Point out each malaria parasite and each leukocyte.
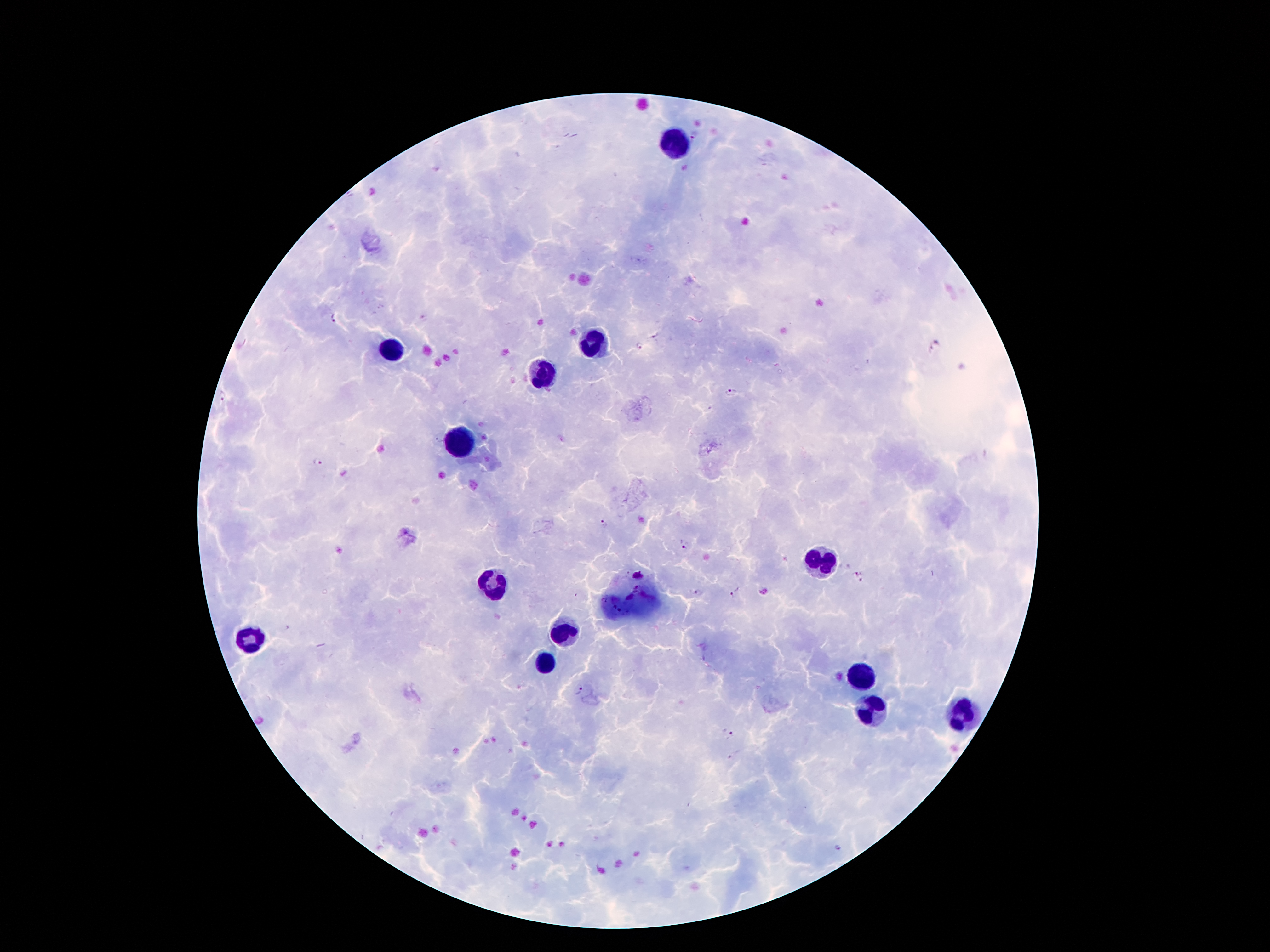

Approximate object centers, in pixels from the top-left corner.
Malaria parasites: (x=694, y=135), (x=335, y=319), (x=658, y=338), (x=640, y=347), (x=730, y=391), (x=222, y=398), (x=317, y=462), (x=603, y=523), (x=683, y=543), (x=856, y=573), (x=735, y=592), (x=698, y=594), (x=579, y=687), (x=731, y=736), (x=840, y=847).
Leukocytes: (x=678, y=143), (x=596, y=341), (x=390, y=353), (x=541, y=378), (x=461, y=446), (x=818, y=559), (x=493, y=584), (x=627, y=599), (x=560, y=630), (x=251, y=639), (x=545, y=664), (x=860, y=677), (x=869, y=710), (x=959, y=714).

Photographed through the microscope eyepiece with a smartphone camera. Giemsa stain. Thick peripheral-blood smear. Patient malaria status: infected with Plasmodium falciparum. 100x magnification. Image is 1270×952 pixels. One field from this slide.